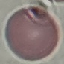
result = no malaria parasites detected
preparation = thin blood smear
image type = cell patch, automatically extracted from a larger field of view and resized to 64 × 64 pixels
capture = smartphone through the microscope eyepiece
stain = Giemsa